Classify this cell by malaria status.
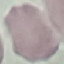
Uninfected.

Giemsa-stained preparation. Photographed with a smartphone camera at the microscope eyepiece. Thin smear of blood. Cell patch, automatically extracted from a larger field of view and resized to 64 × 64 pixels.